Identify the parasite.
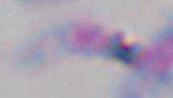

This is Toxoplasma gondii.

Micrograph. Captured at 1000x magnification.